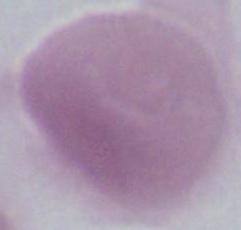

identification = red blood cell
magnification = 1000x
modality = photomicrograph